Classify this cell by malaria status.
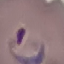

Parasitized.

Summary:
  - Stain: Giemsa
  - Capture: smartphone camera at the microscope eyepiece
  - Image type: automatically extracted cell patch, resized to 64 × 64 pixels
  - Preparation: thin smear